Name the parasite shown.
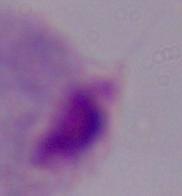

This is a trichomonad.

{
  "modality": "micrograph",
  "magnification": "1000x"
}